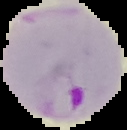
From a thin blood smear. Result: Plasmodium parasites identified. The area outside the segmented cell region is set to black. Image is 127×130 pixels.